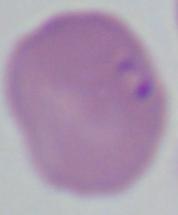
modality = micrograph
identification = Babesia
magnification = 1000x